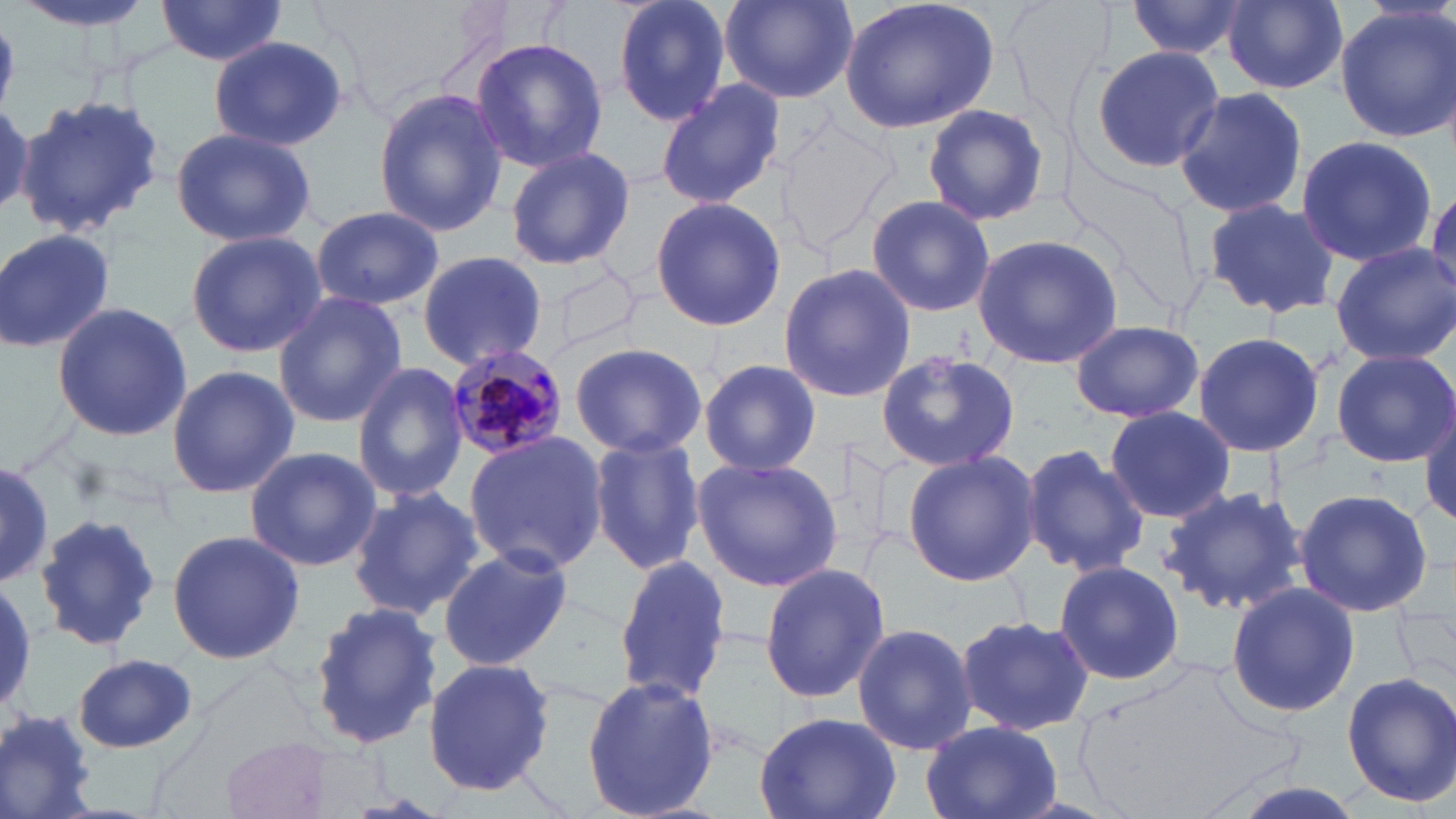

slide-level diagnosis = Plasmodium malariae
field of view = one of a larger specimen
preparation = thin blood smear
magnification = 1000x
stain = May-Grünwald-Giemsa
image size = 1456×819 pixels
Plasmodium malariae-infected red blood cell locations = approximate bounding boxes as [x1, y1, x2, y2] in pixels: [443, 342, 568, 459]
uninfected red blood cell locations = approximate bounding boxes as [x1, y1, x2, y2] in pixels: [9, 0, 166, 34], [155, 0, 288, 67], [612, 0, 733, 129], [720, 0, 855, 103], [838, 0, 1001, 134], [1126, 0, 1247, 60], [1222, 0, 1349, 93], [1335, 3, 1456, 142], [0, 18, 25, 106], [209, 35, 348, 152], [468, 37, 609, 173], [1087, 45, 1225, 174], [655, 80, 784, 209], [372, 87, 511, 236], [1172, 88, 1309, 218], [17, 94, 168, 241], [920, 103, 1052, 227], [170, 126, 318, 246], [1294, 133, 1436, 268], [501, 144, 638, 273], [865, 193, 995, 318], [649, 195, 785, 332], [1203, 196, 1341, 320], [309, 206, 443, 310], [0, 227, 117, 357], [183, 231, 327, 358], [972, 232, 1123, 370], [1328, 243, 1456, 366], [415, 251, 549, 372], [778, 261, 919, 404], [273, 292, 407, 429], [52, 302, 191, 442], [1069, 320, 1204, 423], [1192, 331, 1325, 459], [568, 341, 707, 460], [874, 349, 1025, 471], [1331, 349, 1455, 466], [696, 357, 823, 479], [352, 362, 470, 503], [166, 365, 297, 500], [1102, 406, 1237, 523], [1421, 407, 1456, 530], [463, 431, 609, 577], [586, 435, 705, 578], [1016, 443, 1148, 577], [244, 445, 380, 573], [903, 450, 1039, 586], [692, 457, 843, 591], [0, 464, 57, 589], [1159, 484, 1308, 618], [348, 486, 487, 622], [1292, 488, 1434, 616], [30, 513, 164, 655], [166, 529, 305, 665], [439, 546, 575, 672], [614, 555, 733, 705], [1053, 559, 1184, 684], [759, 563, 890, 704], [1225, 582, 1359, 719], [306, 601, 441, 752], [954, 614, 1096, 736], [852, 622, 978, 756], [72, 655, 200, 754], [425, 658, 560, 797], [1341, 670, 1456, 806], [580, 675, 723, 819], [1, 704, 103, 815], [753, 710, 901, 819], [921, 719, 1062, 819], [222, 734, 336, 817]
modality = light microscopy